Outline each blood parasite and name the species.
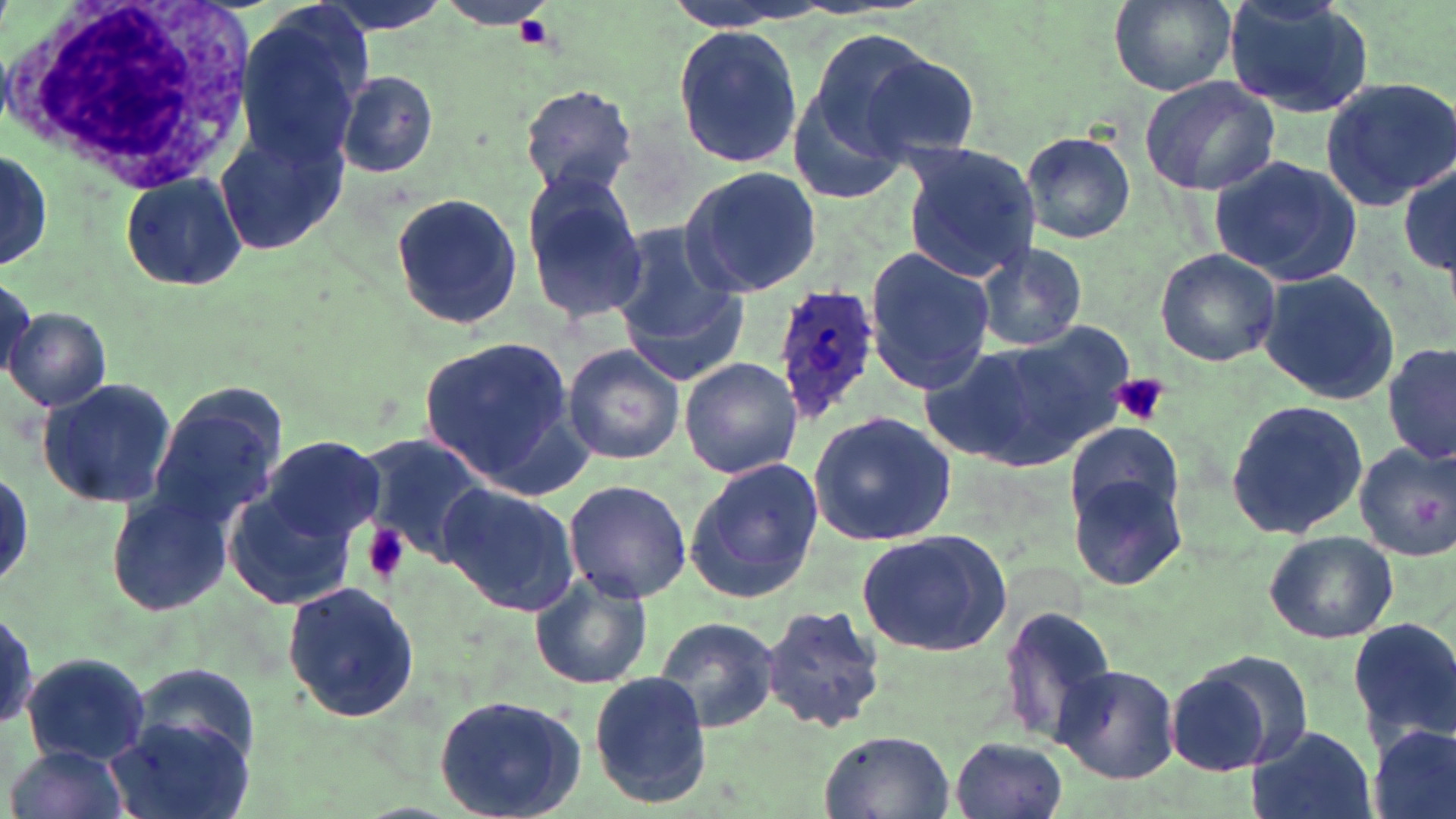

Approximate bounding boxes as (x1,y1)-(x2,y2) corner pairs in pixels.
Plasmodium ovale-infected red blood cells: (769,281)-(882,425).
No Plasmodium falciparum, Plasmodium malariae, Plasmodium vivax, Babesia divergens, or Trypanosoma brucei observed.

slide-level diagnosis = Plasmodium ovale
modality = optical microscopy
stain = May-Grünwald-Giemsa
field of view = one of a larger specimen
image size = 1456×819 pixels
preparation = thin blood film
platelet locations = approximate bounding boxes as (x1,y1)-(x2,y2) corner pairs in pixels: (516,15)-(553,50), (1112,373)-(1168,426), (364,521)-(409,586)
uninfected red blood cell locations = approximate bounding boxes as (x1,y1)-(x2,y2) corner pairs in pixels: (310,0)-(457,37), (1108,0)-(1236,96), (1220,0)-(1376,116), (231,12)-(369,167), (672,23)-(804,167), (847,43)-(982,163), (337,70)-(438,179), (1137,73)-(1282,198), (1321,76)-(1456,209), (519,83)-(640,199), (788,89)-(910,207), (215,126)-(347,255), (1021,132)-(1136,243), (900,143)-(1042,283), (0,147)-(54,271), (1206,154)-(1363,286), (1399,161)-(1456,281), (680,165)-(822,300), (120,170)-(248,288), (521,174)-(650,325), (391,191)-(521,330), (615,223)-(744,386), (974,243)-(1089,352), (1154,247)-(1282,367), (864,248)-(995,396), (1259,269)-(1399,405), (0,274)-(37,382), (5,307)-(110,412), (928,331)-(1126,471), (416,337)-(582,486), (562,341)-(685,467), (1383,341)-(1455,466), (678,356)-(804,479), (36,375)-(175,510), (145,387)-(285,531), (1227,400)-(1370,541), (809,411)-(959,545), (1066,421)-(1183,531), (359,436)-(492,566), (261,440)-(387,550), (1353,441)-(1456,562), (685,458)-(823,605), (222,460)-(378,615), (1066,470)-(1190,591), (563,479)-(692,604), (438,483)-(580,614), (108,490)-(235,615), (856,527)-(1012,655), (1264,531)-(1398,643), (529,571)-(653,690), (282,580)-(421,727), (0,602)-(38,739), (762,602)-(888,736), (1000,603)-(1121,746), (655,616)-(781,733), (1348,616)-(1456,746), (20,650)-(152,764), (1164,658)-(1298,777), (1052,662)-(1180,785), (131,664)-(259,764), (589,673)-(711,805), (432,692)-(589,819), (105,716)-(251,819), (1369,722)-(1455,819), (1243,724)-(1377,819), (818,730)-(955,819), (952,736)-(1068,819), (7,744)-(130,819)
magnification = 1000x
white blood cell locations = approximate bounding boxes as (x1,y1)-(x2,y2) corner pairs in pixels: (0,0)-(262,192)